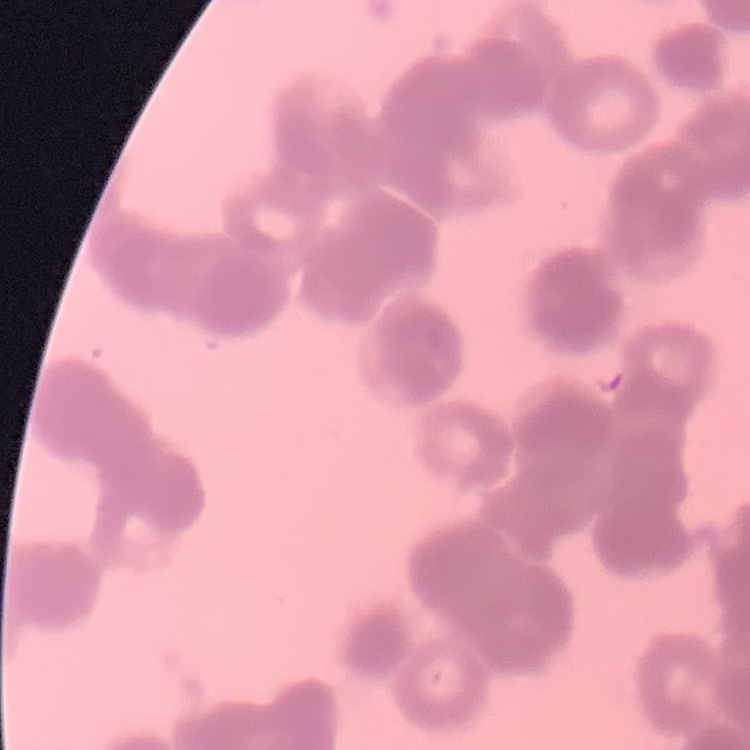

red blood cell morphology = rouleaux formation
preparation = thin peripheral smear
stain = Field's or Giemsa
image type = one tile cut from a larger photomicrograph